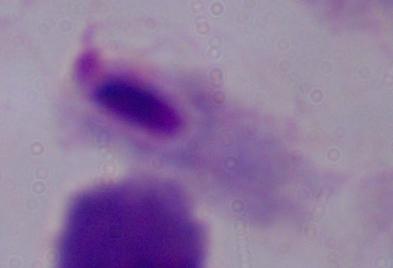

Micrograph. 1000x magnification. A trichomonad is seen.